Assess this cell for malaria.
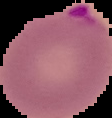
It is parasitized.

image type = segmented cell region with the area outside set to black
preparation = thin blood smear
image size = 112×118 pixels